Point out each malaria parasite.
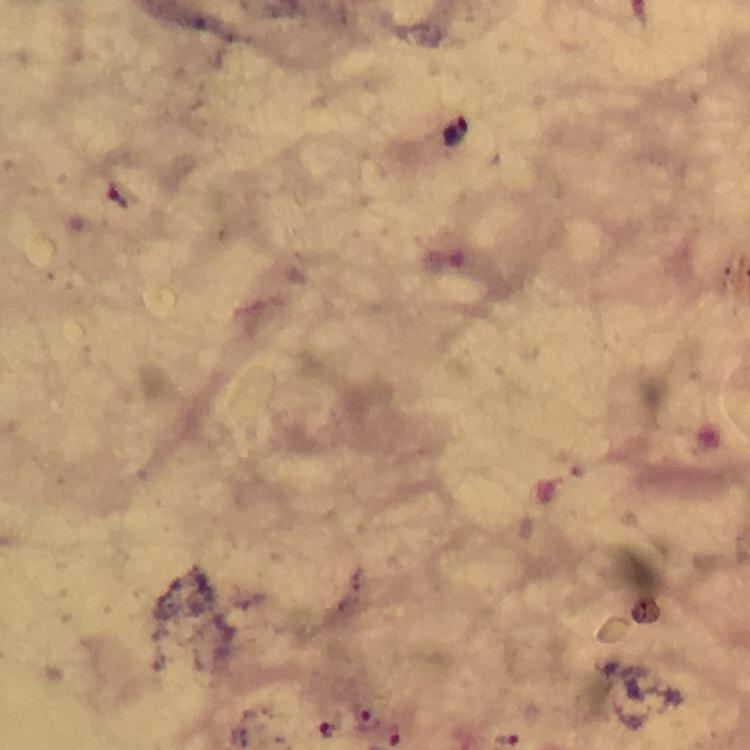
Approximate object centers, in pixels from the top-left corner.
Malaria parasites: (x=366, y=719), (x=327, y=729), (x=392, y=736).

immersion oil = applied
stain = Giemsa
context = from a malaria diagnostic workup
magnification = 100x
capture = smartphone camera through the microscope
preparation = thick blood film
cropped from = a single field of view
image size = 750×750 pixels